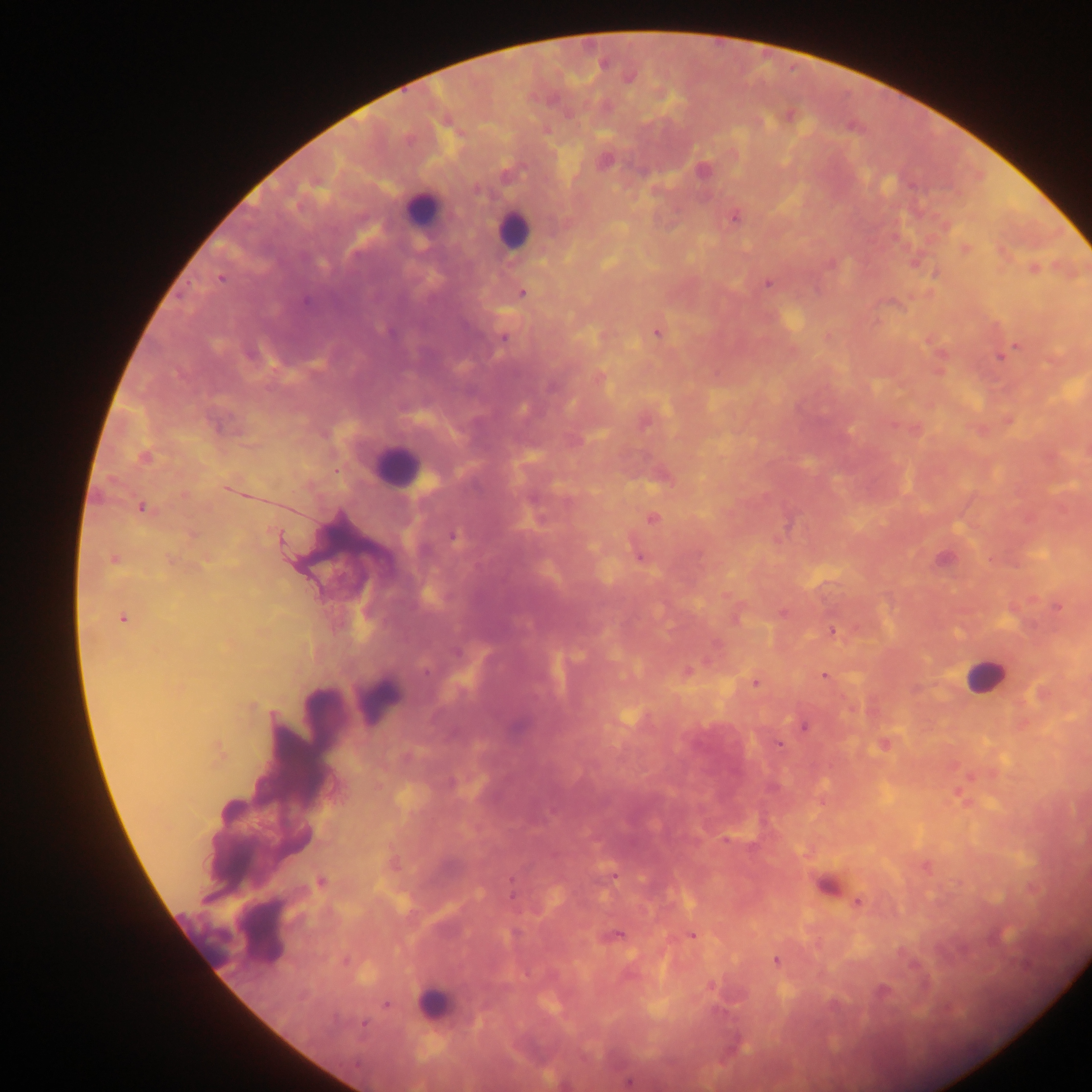
Approximate centers as [x, y] in pixels. Leukocyte locations: [422, 210], [513, 230], [395, 467], [985, 675], [378, 700], [826, 884], [260, 932], [205, 938], [433, 1005]. Plasmodium parasite locations: [628, 76], [789, 115], [604, 162], [702, 171], [733, 216], [965, 248], [915, 262], [1033, 268], [935, 273], [767, 282], [521, 293], [657, 332], [828, 335], [503, 337], [1017, 345], [999, 357], [599, 376], [1008, 419], [644, 420], [914, 428], [144, 457], [662, 475], [142, 507], [652, 517], [454, 535], [638, 554], [114, 559], [944, 559], [1057, 605], [782, 612], [123, 618], [832, 630], [687, 671], [825, 675], [755, 682], [804, 725], [778, 743], [884, 744], [218, 753], [958, 793], [925, 866], [614, 875], [320, 883], [858, 902], [691, 934], [615, 935], [776, 959], [711, 985], [628, 1080]. Mobile-phone photograph taken through the microscope. Image is 1092×1092 pixels. Thick blood smear. Single field of view. Collected in Ghana.